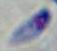

{
  "identification": "Toxoplasma gondii",
  "modality": "photomicrograph",
  "magnification": "1000x"
}